Mark where platelets are.
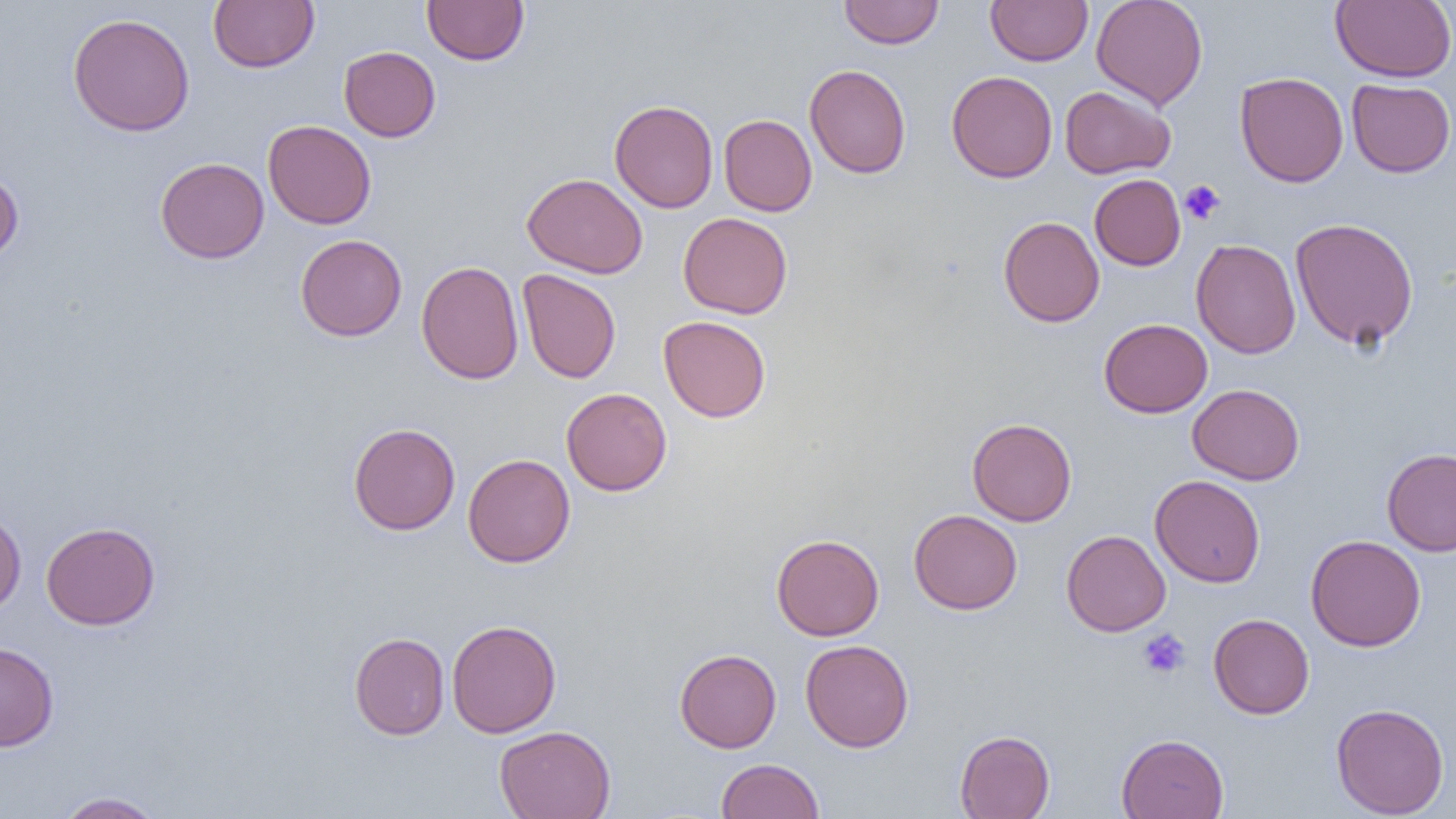
Approximate bounding boxes as (x1,y1)-(x2,y2) corner pairs in pixels.
Platelets: (1179,179)-(1226,225), (1137,629)-(1191,679).

Summary:
  - Uninfected red blood cell locations: (208,0)-(319,73), (422,0)-(529,66), (985,0)-(1093,66), (1091,0)-(1208,110), (1331,0)-(1456,82), (839,1)-(944,49), (67,13)-(195,137), (339,46)-(441,141), (804,63)-(911,178), (946,70)-(1058,183), (1235,71)-(1348,187), (1346,78)-(1456,178), (1060,86)-(1175,179), (609,99)-(719,213), (719,114)-(817,216), (263,120)-(376,229), (155,157)-(269,263), (0,170)-(24,265), (522,173)-(648,278), (1089,174)-(1186,271), (679,212)-(793,319), (998,216)-(1104,327), (1290,217)-(1419,350), (295,234)-(407,341), (1191,238)-(1301,359), (416,260)-(524,384), (517,268)-(622,384), (658,315)-(771,422), (1099,318)-(1212,417), (1187,383)-(1304,485), (561,387)-(672,496), (967,418)-(1077,526), (348,422)-(460,535), (1382,447)-(1456,556), (463,453)-(575,568), (1150,474)-(1265,588), (0,508)-(26,617), (909,509)-(1022,614), (40,521)-(160,630), (1061,530)-(1171,636), (771,533)-(884,641), (1305,534)-(1426,651), (1208,613)-(1314,719), (447,619)-(562,738), (349,632)-(450,740), (800,639)-(914,752), (0,642)-(59,752), (675,648)-(781,752), (1331,702)-(1449,818), (494,725)-(616,819), (955,730)-(1055,818), (1116,733)-(1229,819), (716,758)-(824,818), (54,791)-(166,818)
  - Slide-level diagnosis: negative for blood parasites
  - Image size: 1456×819 pixels
  - Modality: light microscopy
  - Preparation: thin blood film
  - Magnification: 1000x
  - Field of view: one of a larger specimen